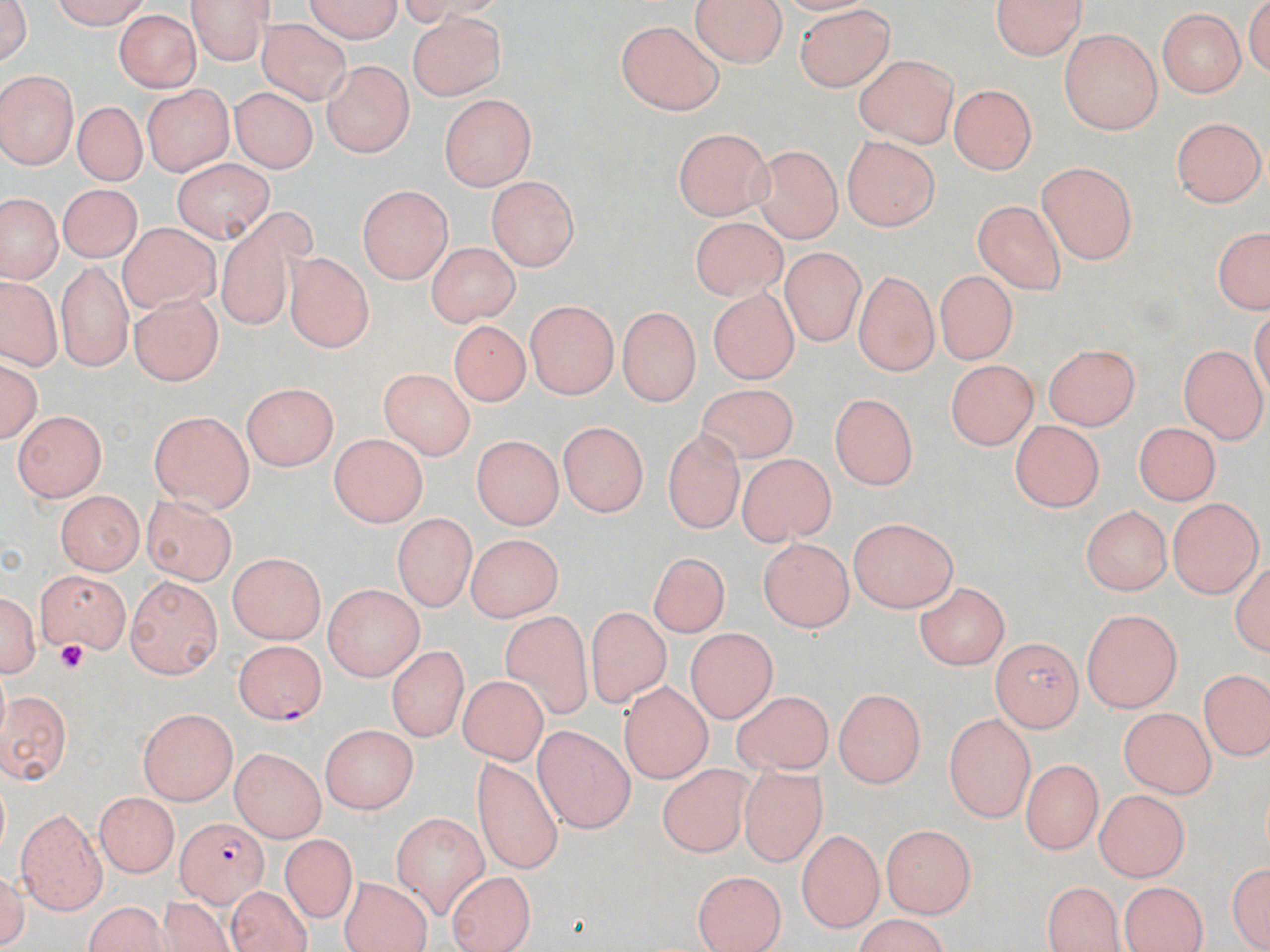

Summary:
  - Coordinate format: approximate bounding boxes as [x1, y1, x2, y2] in pixels
  - Uninfected red blood cell locations: [1, 0, 36, 71], [45, 0, 155, 27], [189, 0, 275, 62], [298, 0, 407, 40], [990, 0, 1088, 61], [691, 1, 786, 67], [794, 3, 896, 92], [1157, 6, 1247, 99], [114, 13, 202, 95], [409, 13, 507, 102], [257, 19, 351, 104], [616, 20, 726, 115], [1059, 29, 1165, 135], [854, 53, 958, 148], [321, 59, 415, 158], [0, 71, 77, 170], [142, 82, 231, 176], [950, 83, 1037, 175], [232, 85, 316, 174], [437, 95, 534, 191], [73, 102, 147, 187], [1173, 116, 1264, 209], [670, 128, 776, 216], [840, 134, 941, 229], [748, 142, 842, 241], [168, 156, 274, 241], [1035, 160, 1135, 264], [488, 174, 578, 268], [357, 184, 453, 287], [57, 186, 139, 263], [974, 197, 1070, 292], [3, 199, 60, 281], [209, 203, 325, 338], [682, 211, 794, 303], [117, 224, 218, 313], [1209, 226, 1269, 318], [423, 242, 522, 324], [778, 249, 879, 344], [286, 253, 372, 352], [45, 258, 141, 374], [932, 269, 1022, 360], [852, 270, 935, 375], [3, 281, 57, 373], [708, 289, 798, 383], [127, 292, 222, 385], [526, 298, 618, 397], [613, 306, 699, 408], [450, 321, 529, 408], [1045, 341, 1141, 431], [1180, 346, 1265, 441], [1, 357, 40, 448], [947, 357, 1038, 445], [379, 368, 478, 459], [242, 383, 338, 469], [692, 387, 799, 463], [827, 387, 922, 488], [14, 410, 108, 500], [145, 412, 255, 509], [558, 419, 653, 515], [1008, 419, 1104, 511], [1132, 423, 1220, 507], [659, 430, 744, 535], [328, 434, 428, 525], [468, 441, 557, 530], [736, 449, 837, 543], [52, 491, 142, 577], [138, 493, 239, 581], [1168, 497, 1257, 597], [1083, 506, 1169, 596], [392, 511, 475, 613], [848, 516, 958, 613], [466, 537, 559, 624], [760, 540, 852, 632], [643, 551, 729, 643], [227, 555, 327, 644], [31, 570, 128, 651], [121, 578, 222, 679], [324, 580, 423, 681], [0, 583, 39, 684], [913, 584, 1007, 669], [588, 608, 674, 712], [505, 609, 593, 719], [1080, 609, 1180, 711], [685, 628, 779, 723], [992, 638, 1082, 730], [388, 643, 469, 744], [459, 673, 549, 761], [1201, 673, 1267, 758], [617, 683, 712, 785], [1, 686, 74, 787], [833, 688, 925, 789], [728, 691, 839, 778], [1119, 704, 1216, 798], [137, 706, 240, 803], [944, 714, 1033, 819], [534, 721, 634, 833], [322, 723, 419, 814], [228, 747, 328, 837], [471, 756, 559, 871], [1024, 760, 1098, 854], [656, 764, 754, 857], [734, 764, 832, 871], [1094, 790, 1189, 878], [95, 792, 176, 875], [16, 808, 109, 912], [392, 810, 490, 912], [883, 826, 974, 919], [797, 832, 885, 928], [279, 834, 355, 922], [1226, 861, 1269, 949], [691, 869, 786, 952], [446, 874, 539, 952], [340, 878, 434, 950], [1042, 879, 1127, 952], [1120, 881, 1207, 952], [226, 886, 317, 951], [159, 895, 242, 952], [84, 903, 181, 952], [848, 917, 955, 951]
  - Plasmodium falciparum-infected red blood cell locations: [231, 638, 329, 722], [174, 816, 265, 903]
  - Platelet locations: [51, 641, 89, 670]
  - Slide-level diagnosis: Plasmodium falciparum
  - Image size: 1270×952 pixels
  - Modality: light microscopy
  - Magnification: 1000x
  - Preparation: thin blood smear
  - Stain: May-Grünwald-Giemsa
  - Field of view: one of a larger specimen